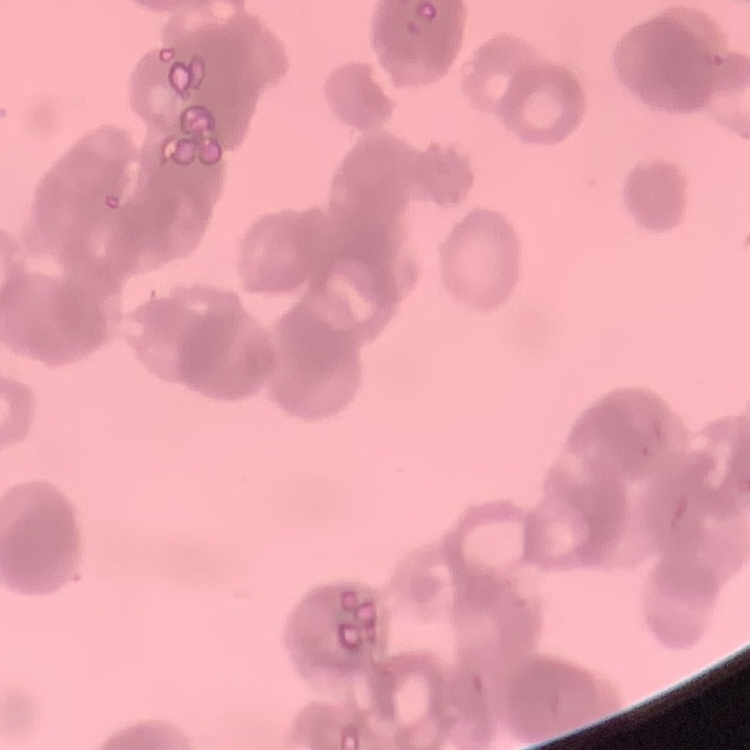
{
  "erythrocyte_morphology": "rouleaux formation",
  "image_type": "one tile cut from a larger photomicrograph",
  "preparation": "thin peripheral smear",
  "stain": "Field's or Giemsa"
}